Assess this cell for malaria.
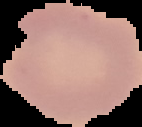

Uninfected.

From a thin blood smear. Segmented cell region on a black background. Image is 142×127 pixels.